Report the malaria status of this cell.
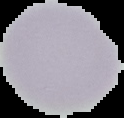
Uninfected.

The area outside the segmented cell region is set to black. Image is 124×118 pixels. From a thin blood film.